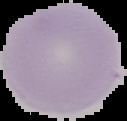

preparation = thin blood smear
malaria status = uninfected
image size = 127×121 pixels
image type = segmented cell region with the area outside set to black